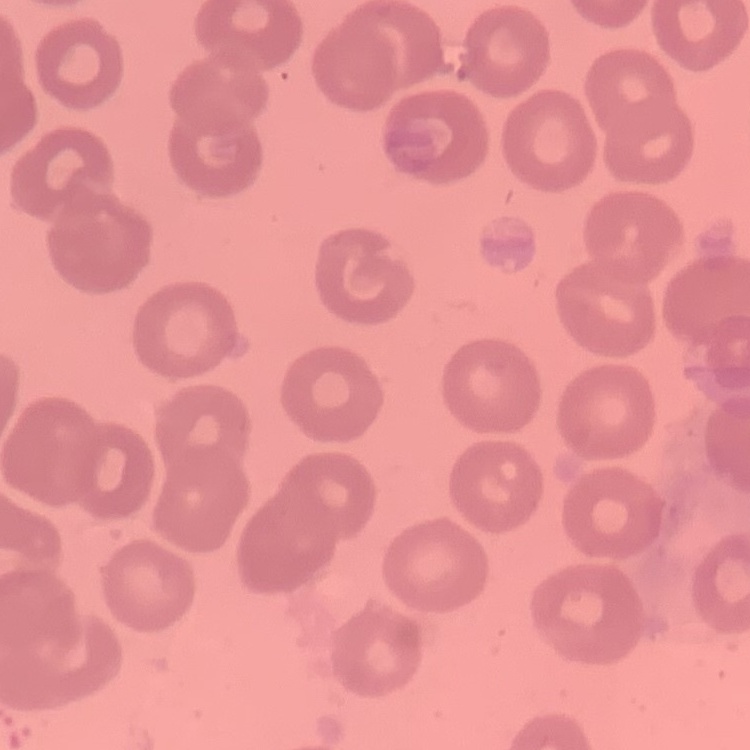
The red blood cells exhibit no rouleaux formation. Field's or Giemsa stain. One tile cut from a larger photomicrograph. Thin blood smear.